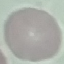

Malaria status: uninfected. Cell patch, automatically extracted from a larger field of view and resized to 64 × 64 pixels. Photographed with a smartphone camera at the microscope eyepiece. Thin smear of blood. Giemsa-stained preparation.